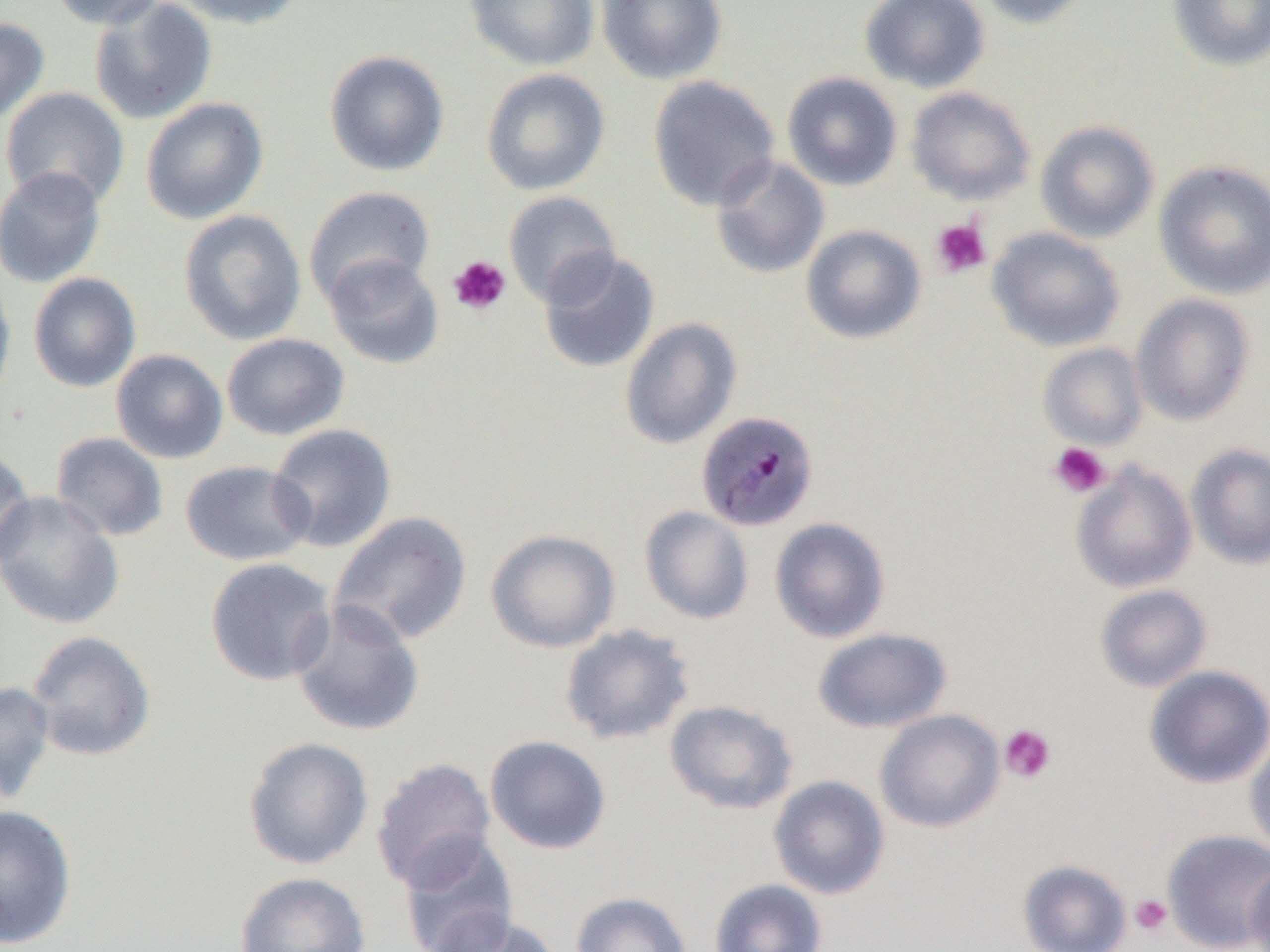
Plasmodium malariae-infected red blood cell locations = approximate bounding boxes as (x1, y1, x2, y2) in pixels: (696, 409, 819, 532)
slide-level diagnosis = Plasmodium malariae
field of view = single
magnification = 1000x
modality = optical microscopy
image size = 1270×952 pixels
preparation = thin blood film
uninfected red blood cell locations = approximate bounding boxes as (x1, y1, x2, y2) in pixels: (48, 0, 165, 29), (175, 0, 308, 29), (465, 0, 599, 70), (596, 0, 728, 85), (860, 0, 990, 93), (975, 0, 1096, 29), (1168, 0, 1270, 71), (89, 1, 218, 124), (0, 16, 50, 124), (324, 50, 450, 177), (481, 68, 611, 195), (782, 72, 903, 191), (647, 76, 781, 212), (1, 86, 130, 209), (906, 87, 1035, 205), (140, 97, 269, 225), (1035, 120, 1159, 243), (710, 156, 830, 279), (1153, 160, 1270, 299), (0, 165, 106, 288), (304, 186, 435, 306), (503, 191, 621, 307), (179, 209, 307, 345), (801, 224, 927, 344), (986, 227, 1125, 352), (538, 250, 660, 373), (323, 254, 445, 370), (0, 271, 17, 413), (28, 272, 141, 392), (1130, 294, 1256, 426), (619, 317, 742, 450), (221, 333, 350, 441), (1038, 343, 1148, 451), (111, 349, 229, 464), (267, 423, 397, 553), (51, 432, 169, 542), (1186, 443, 1270, 570), (0, 445, 36, 567), (180, 460, 314, 567), (1070, 461, 1196, 593), (0, 490, 125, 629), (640, 505, 754, 625), (329, 511, 473, 647), (769, 517, 890, 643), (485, 528, 620, 653), (205, 557, 337, 686), (1095, 584, 1212, 692), (290, 599, 425, 737), (560, 624, 694, 745), (813, 627, 951, 732), (25, 630, 156, 761), (1144, 665, 1270, 788), (0, 681, 56, 806), (665, 700, 798, 814), (875, 709, 1005, 832), (1245, 734, 1270, 860), (485, 735, 611, 854), (243, 737, 374, 870), (371, 758, 496, 891), (768, 775, 890, 899), (0, 804, 78, 949), (1162, 829, 1270, 952), (398, 833, 520, 952), (1017, 860, 1131, 952), (1244, 862, 1270, 952), (234, 871, 371, 952), (710, 878, 827, 952), (571, 891, 692, 952), (428, 911, 562, 952)
platelet locations = approximate bounding boxes as (x1, y1, x2, y2) in pixels: (931, 218, 991, 278), (448, 255, 511, 315), (1049, 442, 1111, 498), (999, 724, 1056, 784), (1130, 894, 1172, 936)